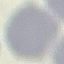
malaria status = uninfected
image type = automatically extracted cell patch, resized to 64 × 64 pixels
preparation = thin blood film
stain = Giemsa
capture = smartphone through the microscope eyepiece